Report the malaria status of this cell.
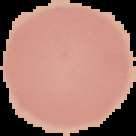

It is uninfected.

Image is 136×136 pixels. From a thin blood smear. Segmented cell region on a black background.